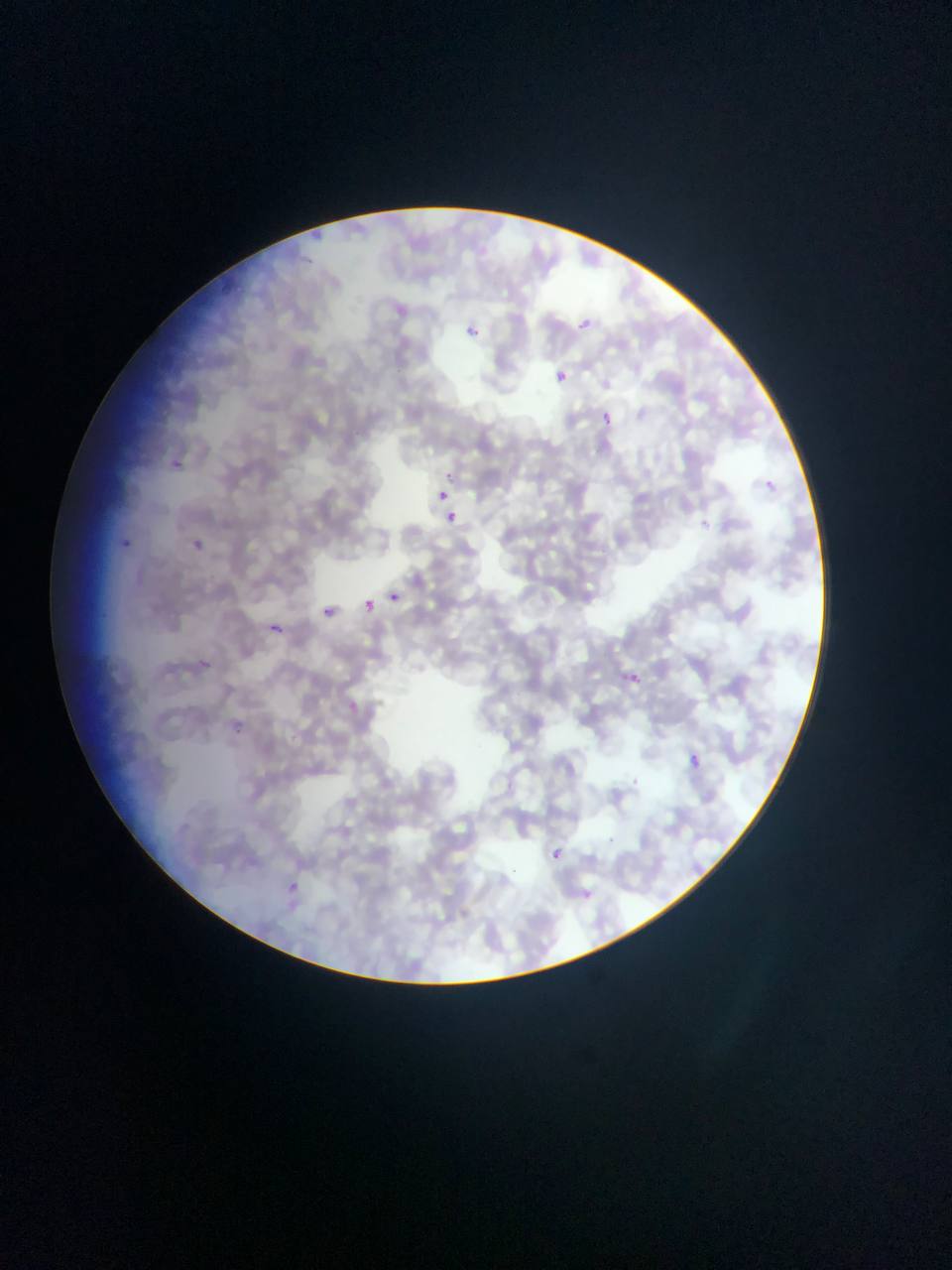

field of view = single
preparation = thin blood smear
image size = 952×1270 pixels
Plasmodium parasite locations = approximate bounding boxes as (left, top, right, bottom) in pixels: (578, 318, 592, 332), (462, 327, 497, 344), (555, 369, 571, 385), (603, 409, 615, 430), (173, 459, 191, 482), (438, 489, 447, 497), (443, 508, 459, 523), (123, 539, 133, 551), (190, 539, 204, 554), (389, 588, 403, 604), (367, 598, 377, 614), (326, 602, 339, 618), (264, 622, 289, 639), (199, 656, 212, 669), (630, 674, 642, 684), (232, 721, 240, 737), (692, 754, 706, 774), (549, 848, 562, 859), (288, 879, 298, 894)
capture = mobile-phone photograph through a microscope
country = Ghana